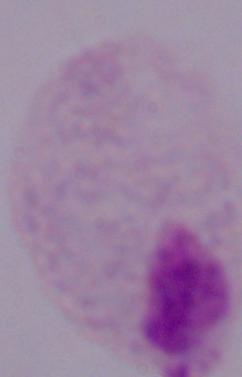

modality = micrograph
identification = trichomonad
magnification = 1000x